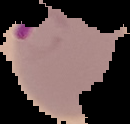

image_type: segmented cell region with the area outside set to black
image_size: 130×124 pixels
preparation: thin blood film
malaria_status: parasitized